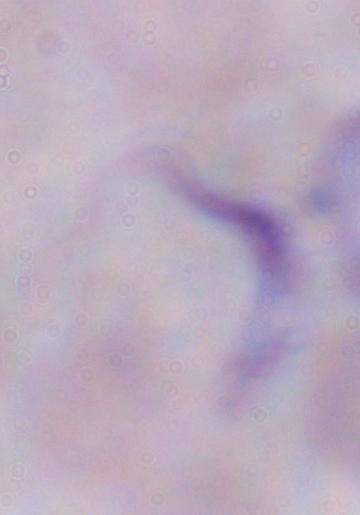
Summary:
  - Modality: photomicrograph
  - Identification: trypanosome
  - Magnification: 1000x